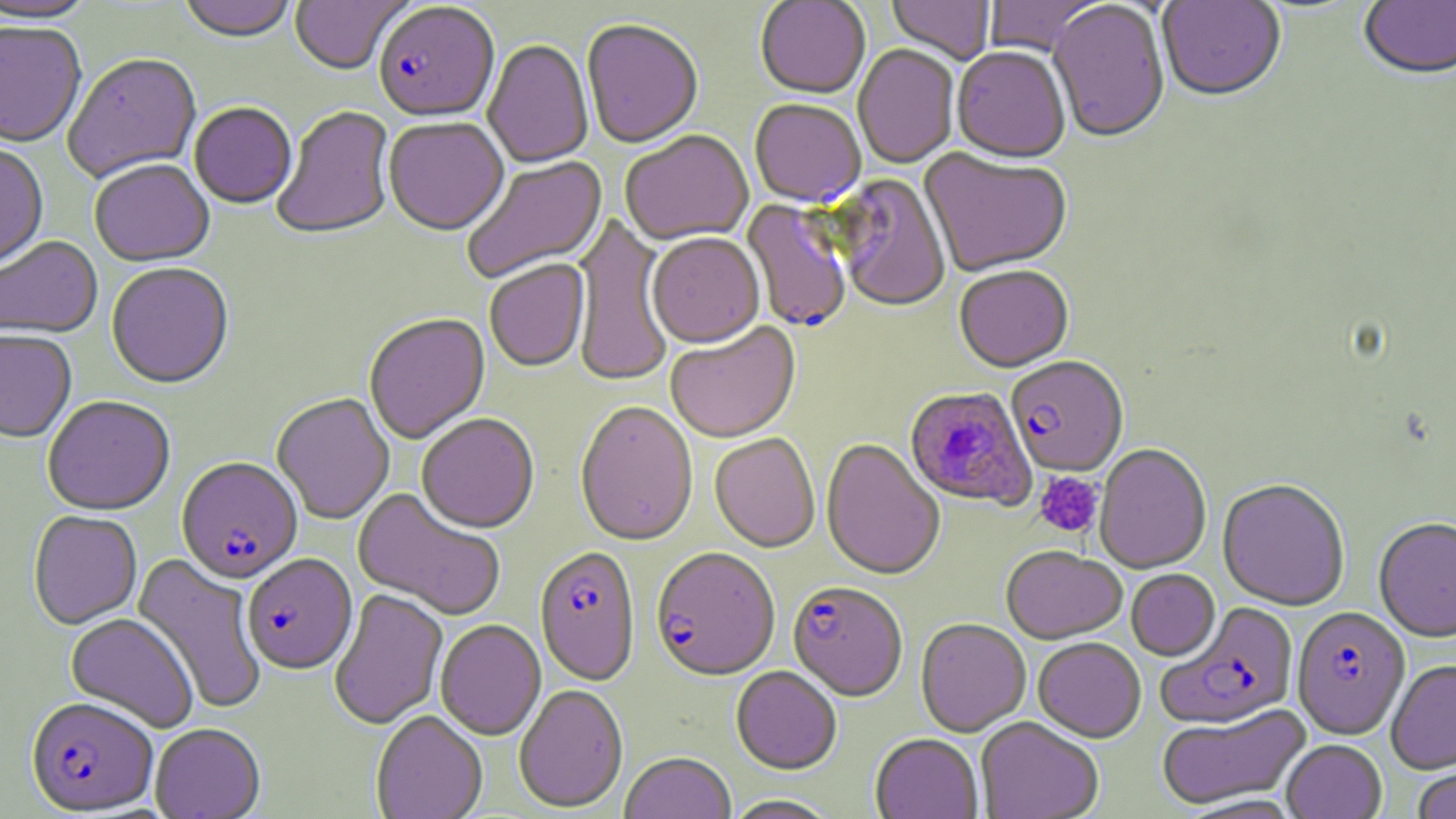
Summary:
  - Coordinate format: approximate bounding boxes as (x1, y1, x2, y2) in pixels
  - Platelet locations: (1033, 472, 1104, 538)
  - Uninfected red blood cell locations: (177, 0, 297, 45), (290, 0, 411, 76), (755, 0, 871, 100), (886, 0, 996, 66), (983, 0, 1106, 57), (1157, 0, 1287, 104), (0, 1, 98, 25), (1358, 1, 1456, 83), (1047, 2, 1171, 146), (582, 22, 703, 151), (0, 23, 87, 150), (482, 41, 594, 169), (853, 45, 959, 170), (952, 49, 1070, 166), (63, 55, 202, 184), (749, 101, 866, 209), (189, 104, 297, 210), (272, 106, 396, 243), (384, 119, 509, 238), (620, 132, 755, 247), (0, 146, 49, 272), (919, 149, 1071, 279), (462, 156, 608, 285), (89, 161, 214, 269), (832, 175, 951, 314), (571, 213, 675, 389), (646, 235, 764, 351), (0, 237, 103, 341), (484, 261, 591, 374), (106, 264, 234, 391), (954, 267, 1074, 375), (364, 314, 490, 445), (665, 324, 802, 445), (0, 332, 76, 445), (272, 394, 394, 525), (43, 397, 174, 517), (574, 403, 698, 549), (417, 415, 539, 536), (709, 435, 820, 554), (821, 440, 945, 582), (1095, 444, 1212, 575), (1217, 480, 1350, 611), (352, 488, 505, 622), (28, 511, 143, 630), (1374, 518, 1456, 643), (1001, 548, 1126, 645), (131, 553, 268, 715), (1126, 570, 1220, 661), (329, 589, 449, 730), (65, 614, 198, 733), (916, 619, 1031, 738), (435, 621, 546, 741), (1033, 638, 1146, 743), (1386, 660, 1456, 775), (731, 667, 842, 776), (514, 686, 628, 814), (1156, 704, 1313, 810), (371, 712, 487, 819), (976, 718, 1103, 819), (150, 725, 265, 819), (870, 735, 983, 819), (1282, 740, 1386, 819), (619, 754, 737, 819), (1412, 761, 1456, 819), (723, 796, 841, 819)
  - Plasmodium falciparum-infected red blood cell locations: (373, 3, 499, 124), (741, 200, 852, 334), (1006, 359, 1128, 478), (904, 386, 1037, 512), (177, 458, 303, 585), (534, 548, 641, 688), (650, 550, 780, 683), (242, 555, 357, 676), (788, 583, 907, 704), (1156, 603, 1299, 729), (1292, 607, 1410, 741), (25, 698, 158, 816)
  - Slide-level diagnosis: Plasmodium falciparum
  - Stain: May-Grünwald-Giemsa
  - Preparation: thin blood film
  - Image size: 1456×819 pixels
  - Modality: light microscopy
  - Magnification: 1000x
  - Field of view: one of a larger specimen